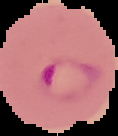
Result: malaria parasites detected. The area outside the segmented cell region is set to black. From a thin blood smear. Image is 118×136 pixels.